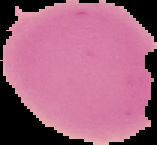

Summary:
  - Preparation: thin blood smear
  - Image type: segmented cell region with the area outside set to black
  - Malaria status: uninfected
  - Image size: 157×145 pixels